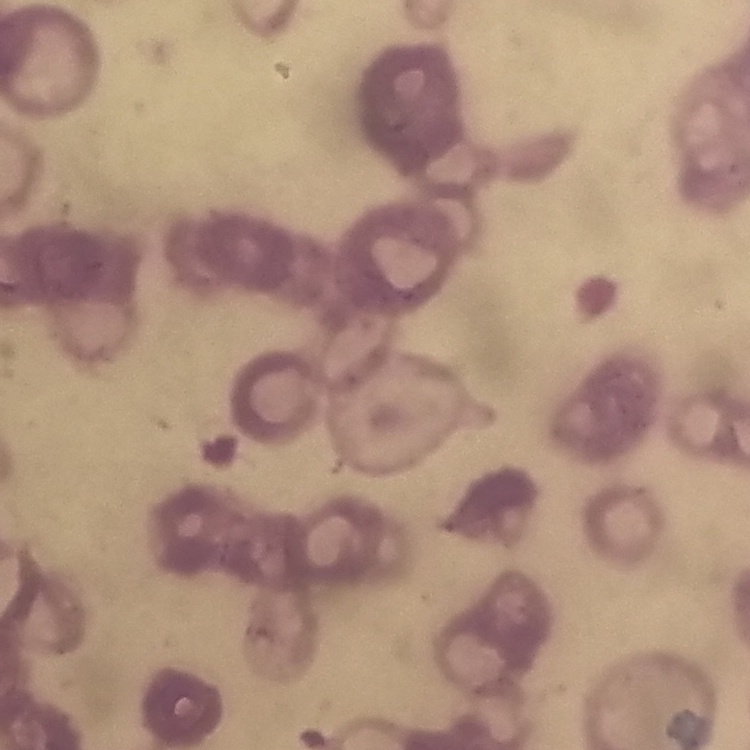
The red blood cells exhibit rouleaux formation. Square crop of a larger photomicrograph. Thin peripheral smear. Stained with either Field's or Giemsa.